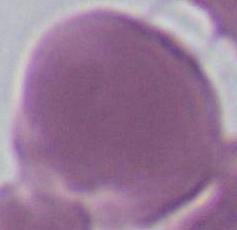

modality: micrograph
identification: red blood cell
magnification: 1000x